State which parasite is depicted.
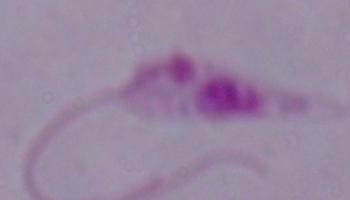
Leishmania.

Captured at 1000x magnification. Micrograph.